Report the malaria status of this cell.
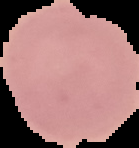
It is uninfected.

Segmented cell region on a black background. Image is 139×148 pixels. From a thin blood film.